Comment on the morphology of the red blood cells.
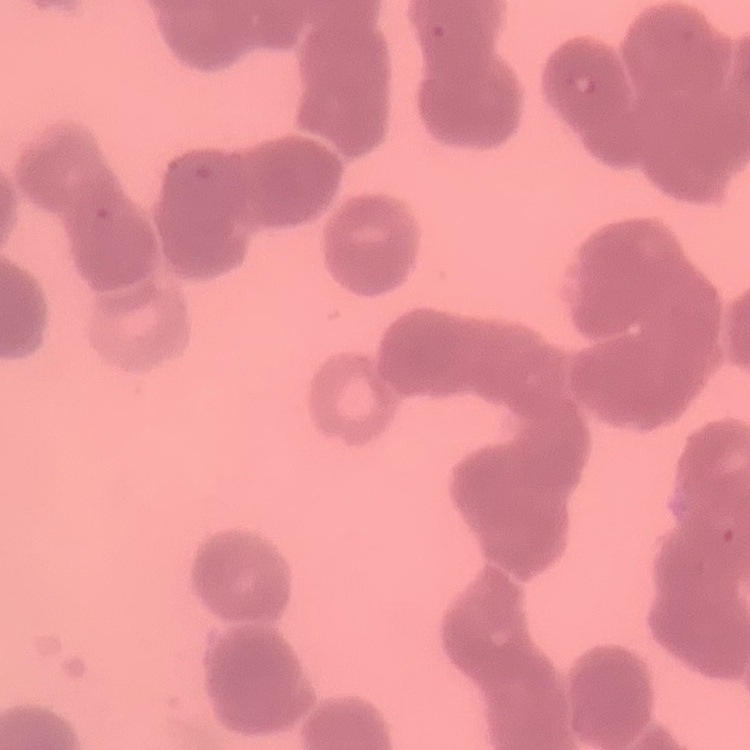
Rouleaux formation.

Summary:
  - Preparation: thin blood film
  - Image type: square crop of a larger photomicrograph
  - Stain: Field's or Giemsa